Assess this cell for malaria.
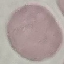
It is uninfected.

Automatically extracted cell patch, resized to 64 × 64 pixels. Acquired by smartphone through the microscope eyepiece. Thin smear of blood. Giemsa stain.